Classify this cell by malaria status.
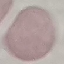
Uninfected.

Cell patch, automatically extracted from a larger field of view and resized to 64 × 64 pixels. Giemsa stain. Thin blood film. Acquired by smartphone through the microscope eyepiece.